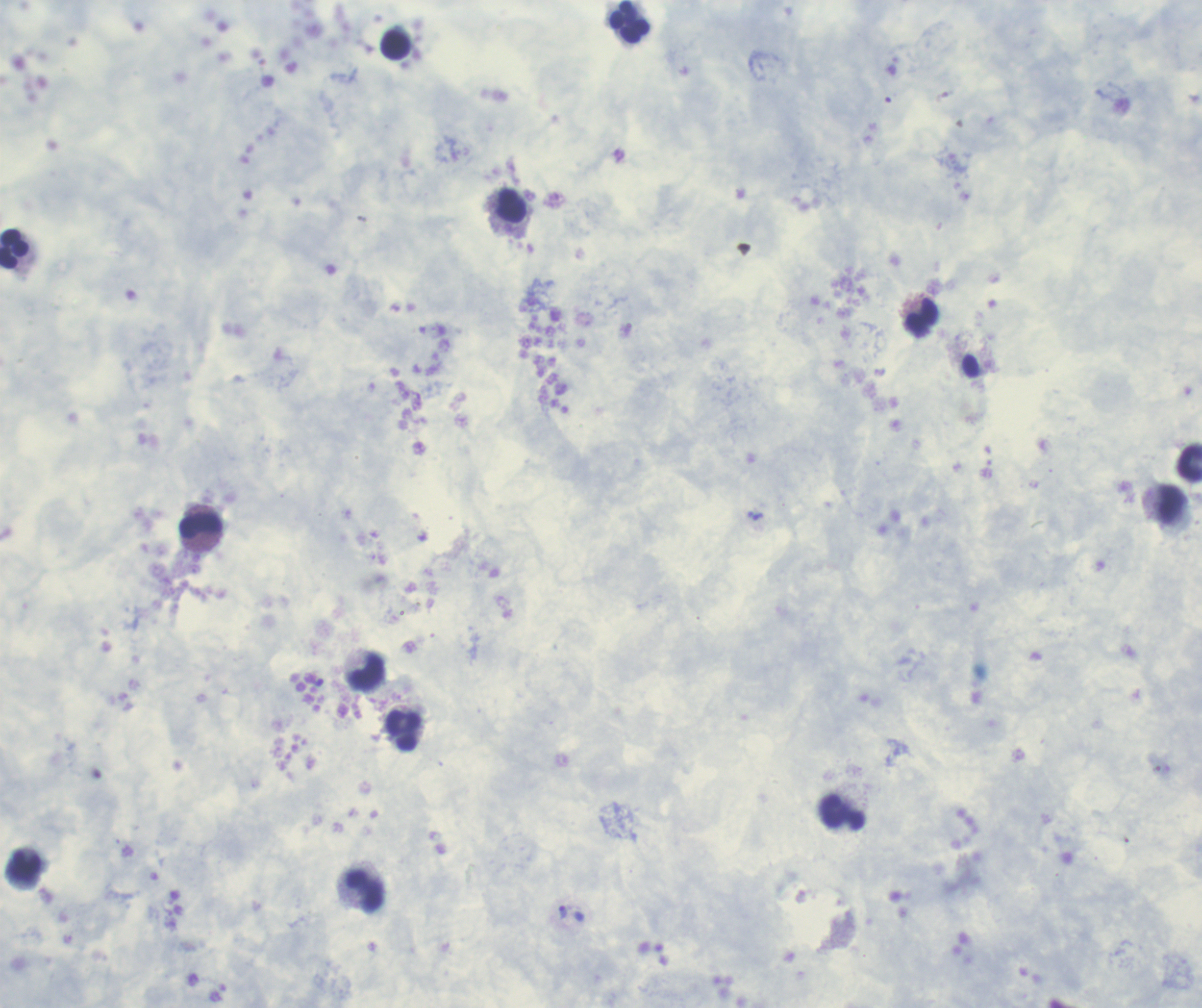

coordinate format = approximate centers as [x, y] in pixels
leukocyte locations = [631, 21], [396, 46], [512, 206], [14, 250], [921, 319], [1190, 463], [1171, 505], [201, 526], [367, 672], [404, 731], [843, 813], [24, 867], [366, 892]
trophozoite locations = [563, 912]
image size = 1202×1008 pixels
result = malaria parasites detected
preparation = thick blood film
background quality = unsatisfactory
magnification = 100x
field of view = single
stain = Romanowsky
context = previously used in a real diagnosis
coloration quality = good